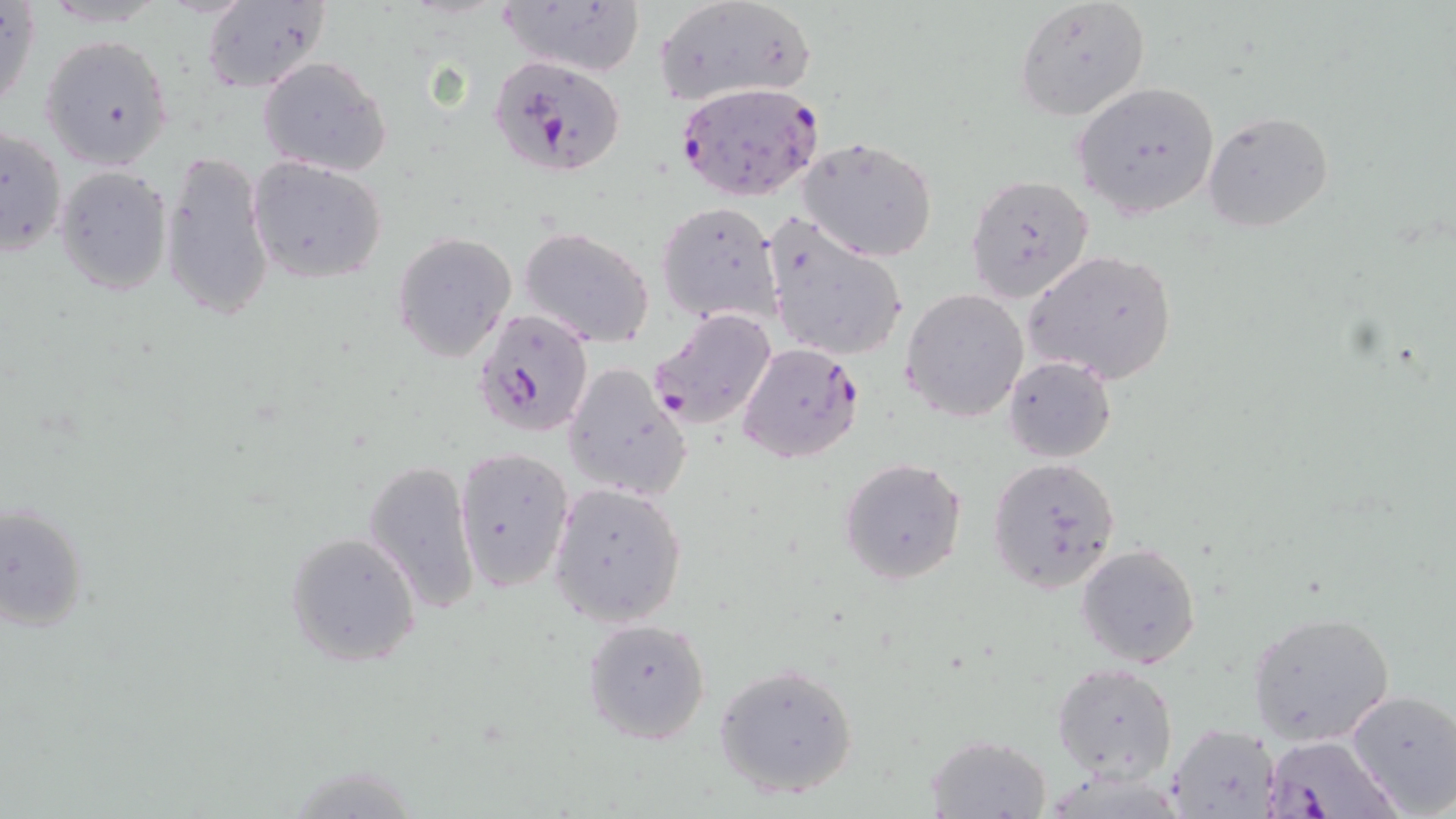
Approximate bounding boxes as (x1,y1)-(x2,y2) corner pairs in pixels. Plasmodium falciparum-infected red blood cell locations: (488,54)-(628,177), (675,83)-(825,202), (473,307)-(596,439), (649,309)-(778,431), (738,342)-(862,465), (1264,734)-(1402,818). Uninfected red blood cell locations: (1,0)-(40,115), (1012,0)-(1151,121), (500,1)-(645,78), (201,2)-(332,92), (652,2)-(817,108), (38,33)-(174,171), (257,56)-(392,177), (1072,80)-(1221,219), (1202,111)-(1334,233), (0,123)-(69,256), (798,137)-(939,262), (159,147)-(275,325), (247,157)-(389,283), (54,164)-(172,297), (965,173)-(1094,303), (657,201)-(783,325), (762,213)-(910,367), (520,226)-(656,348), (392,233)-(516,362), (1024,248)-(1178,384), (901,289)-(1029,423), (1003,355)-(1118,462), (564,362)-(690,500), (453,446)-(574,591), (362,456)-(482,615), (837,456)-(968,586), (986,456)-(1123,594), (550,483)-(687,628), (0,500)-(88,635), (284,531)-(422,669), (1075,543)-(1201,668), (1248,609)-(1397,745), (580,616)-(712,745), (714,661)-(861,799), (1052,663)-(1178,783), (1347,688)-(1456,815), (1165,723)-(1278,817), (924,733)-(1053,818). Slide-level diagnosis: Plasmodium falciparum. 1000x magnification. Thin blood film. Optical microscopy. Image is 1456×819 pixels. May-Grünwald-Giemsa stain. One field of a larger specimen.